Assess this cell for malaria.
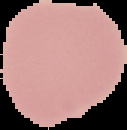

It is uninfected.

Summary:
  - Image size: 127×130 pixels
  - Preparation: thin blood film
  - Image type: segmented cell region on a black background